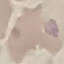
malaria status = uninfected
stain = Giemsa
preparation = thin blood film
image type = automatically extracted cell patch, resized to 64 × 64 pixels
capture = smartphone camera at the microscope eyepiece